State which parasite is depicted.
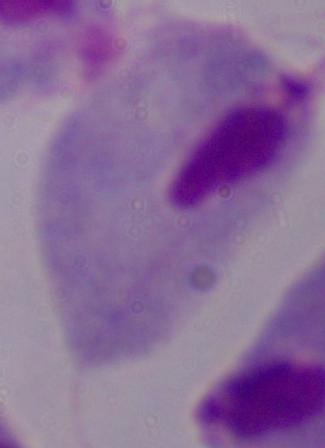
This is a trichomonad.

Summary:
  - Magnification: 1000x
  - Modality: micrograph